Give the position of every Plasmodium parasite visible.
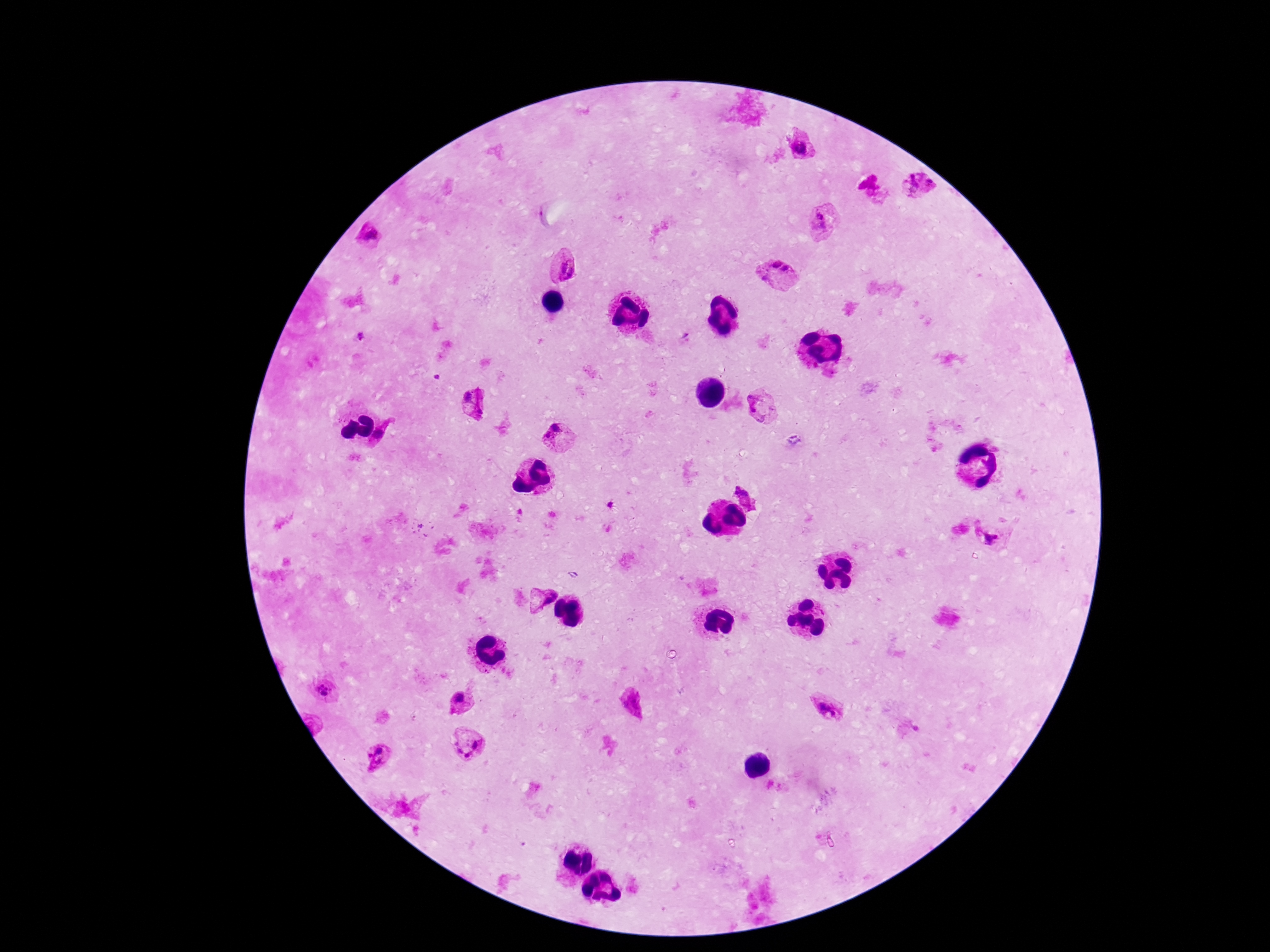
Approximate centers as (x, y) in pixels.
Plasmodium parasites: (801, 149), (920, 185), (818, 221), (366, 238), (563, 265), (778, 274), (476, 404), (758, 406), (386, 437), (559, 438), (744, 494), (990, 537), (542, 597), (325, 691), (460, 700), (631, 703), (824, 706), (466, 746), (379, 756).

Patient malaria status: positive. One field from this slide. Image is 1270×952 pixels. Thick blood smear. Photographed through the microscope eyepiece with a smartphone camera. 100x magnification. Giemsa-stained preparation.